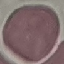
Result: no malaria parasites detected. Cell patch, automatically extracted from a larger field of view and resized to 64 × 64 pixels. Thin blood smear. Photographed with a smartphone camera at the microscope eyepiece. Giemsa stain.